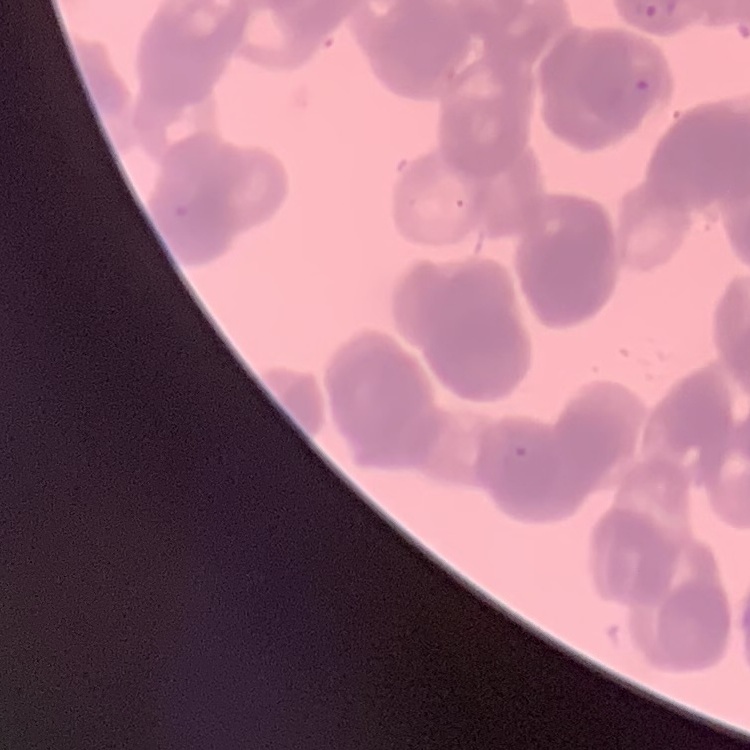
erythrocyte morphology = rouleaux formation
preparation = thin blood film
image type = one tile cut from a larger photomicrograph
stain = Field's or Giemsa